Identify the parasite.
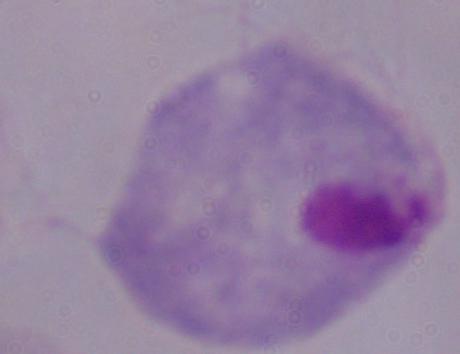
A trichomonad.

Summary:
  - Magnification: 1000x
  - Modality: photomicrograph